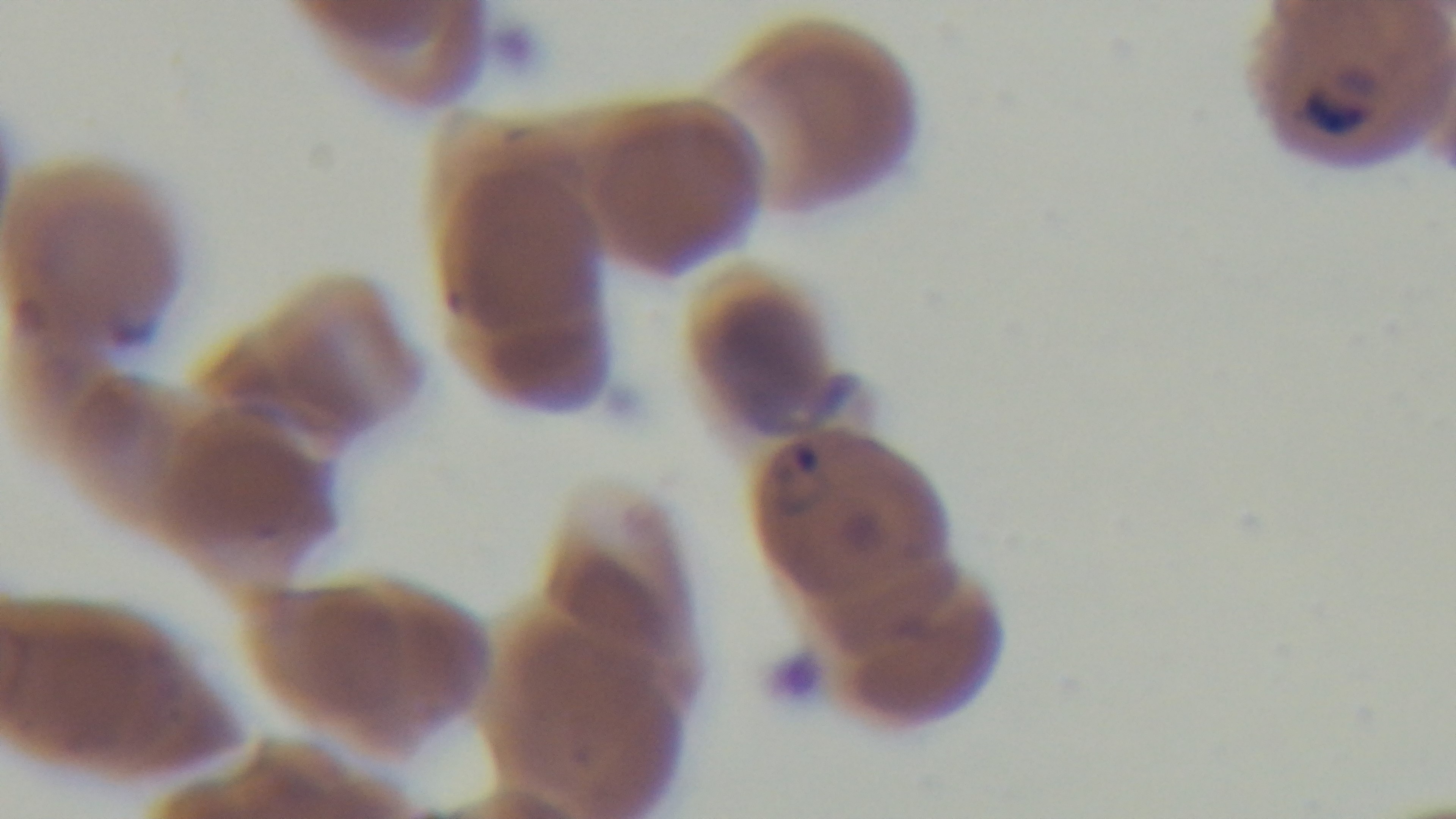

Preparation: thin smear. Malaria status: positive. Single field of view. Photomicrograph. Oil-immersion objective, 100x. Captured with a mounted 4K digital camera. Giemsa-stained.